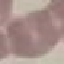

Summary:
  - Malaria status: uninfected
  - Stain: Giemsa
  - Capture: smartphone camera at the microscope eyepiece
  - Image type: cell patch, automatically extracted from a larger field of view and resized to 64 × 64 pixels
  - Preparation: thin blood smear